Outline each Plasmodium vivax-infected red blood cell.
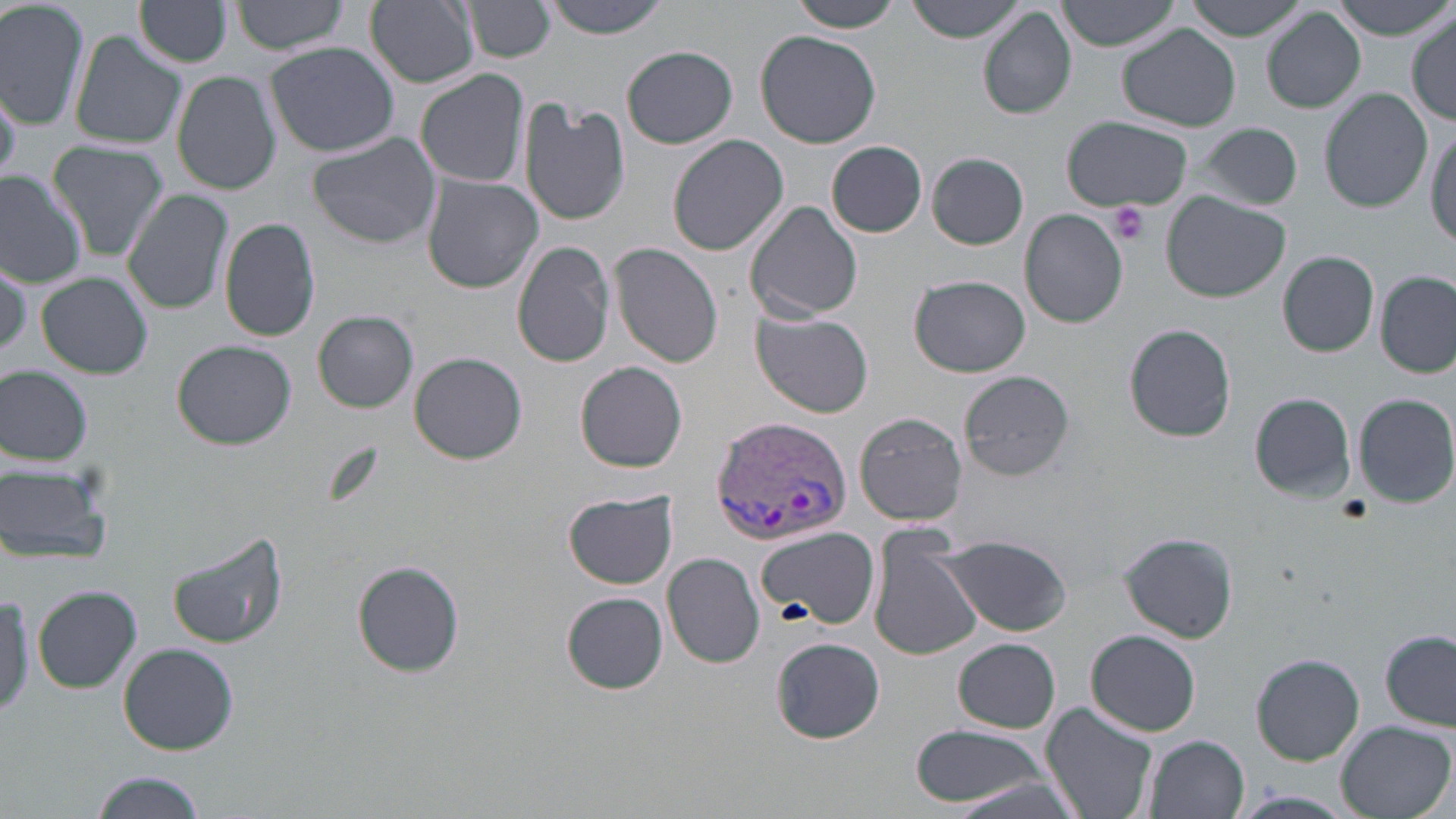
Approximate bounding boxes as [x1, y1, x2, y2] in pixels.
Plasmodium vivax-infected red blood cells: [711, 416, 851, 545].

Platelet locations: [1109, 201, 1150, 244]. Uninfected red blood cell locations: [0, 0, 91, 131], [231, 0, 353, 56], [365, 0, 479, 88], [543, 0, 671, 39], [793, 0, 903, 32], [907, 0, 1029, 42], [1056, 0, 1183, 50], [1188, 0, 1310, 40], [1337, 0, 1453, 38], [469, 1, 555, 61], [137, 2, 233, 66], [978, 7, 1076, 120], [1262, 8, 1366, 113], [1409, 11, 1455, 124], [1119, 26, 1240, 131], [756, 30, 880, 149], [70, 31, 187, 149], [265, 42, 401, 158], [623, 44, 738, 148], [415, 68, 531, 189], [172, 71, 281, 195], [1320, 88, 1431, 212], [519, 98, 631, 226], [1061, 118, 1193, 211], [1190, 121, 1305, 209], [1427, 124, 1456, 249], [306, 133, 441, 249], [668, 134, 789, 256], [45, 141, 170, 261], [827, 141, 927, 237], [928, 153, 1029, 248], [0, 172, 87, 286], [420, 173, 544, 293], [123, 187, 234, 316], [1163, 193, 1293, 304], [744, 201, 862, 324], [1020, 210, 1127, 328], [219, 216, 321, 342], [513, 242, 615, 369], [610, 243, 725, 369], [1278, 251, 1378, 357], [37, 272, 152, 379], [1376, 273, 1454, 376], [911, 275, 1031, 377], [751, 308, 874, 418], [313, 310, 418, 413], [1124, 324, 1236, 441], [172, 340, 296, 450], [410, 353, 528, 465], [575, 362, 688, 474], [0, 365, 93, 465], [958, 370, 1073, 481], [1249, 392, 1357, 502], [1354, 392, 1456, 507], [855, 412, 967, 526], [0, 459, 116, 568], [565, 491, 677, 589], [868, 524, 982, 663], [755, 527, 877, 632], [165, 530, 290, 650], [1118, 531, 1239, 643], [937, 535, 1073, 636], [663, 552, 766, 668], [352, 560, 466, 677], [32, 586, 142, 694], [0, 589, 33, 724], [562, 591, 667, 694], [1087, 629, 1201, 735], [1382, 630, 1456, 731], [771, 637, 885, 743], [954, 638, 1059, 732], [117, 643, 239, 755], [1251, 654, 1365, 765], [1041, 703, 1159, 819], [1334, 721, 1454, 818], [911, 723, 1051, 808], [1146, 734, 1250, 819], [90, 771, 208, 818], [936, 775, 1086, 819], [1230, 790, 1359, 819]. Slide-level diagnosis: Plasmodium vivax. Image is 1456×819 pixels. May-Grünwald-Giemsa stain. Thin blood film. One field of a larger specimen. Optical microscopy. 1000x magnification.